Give the preparation type.
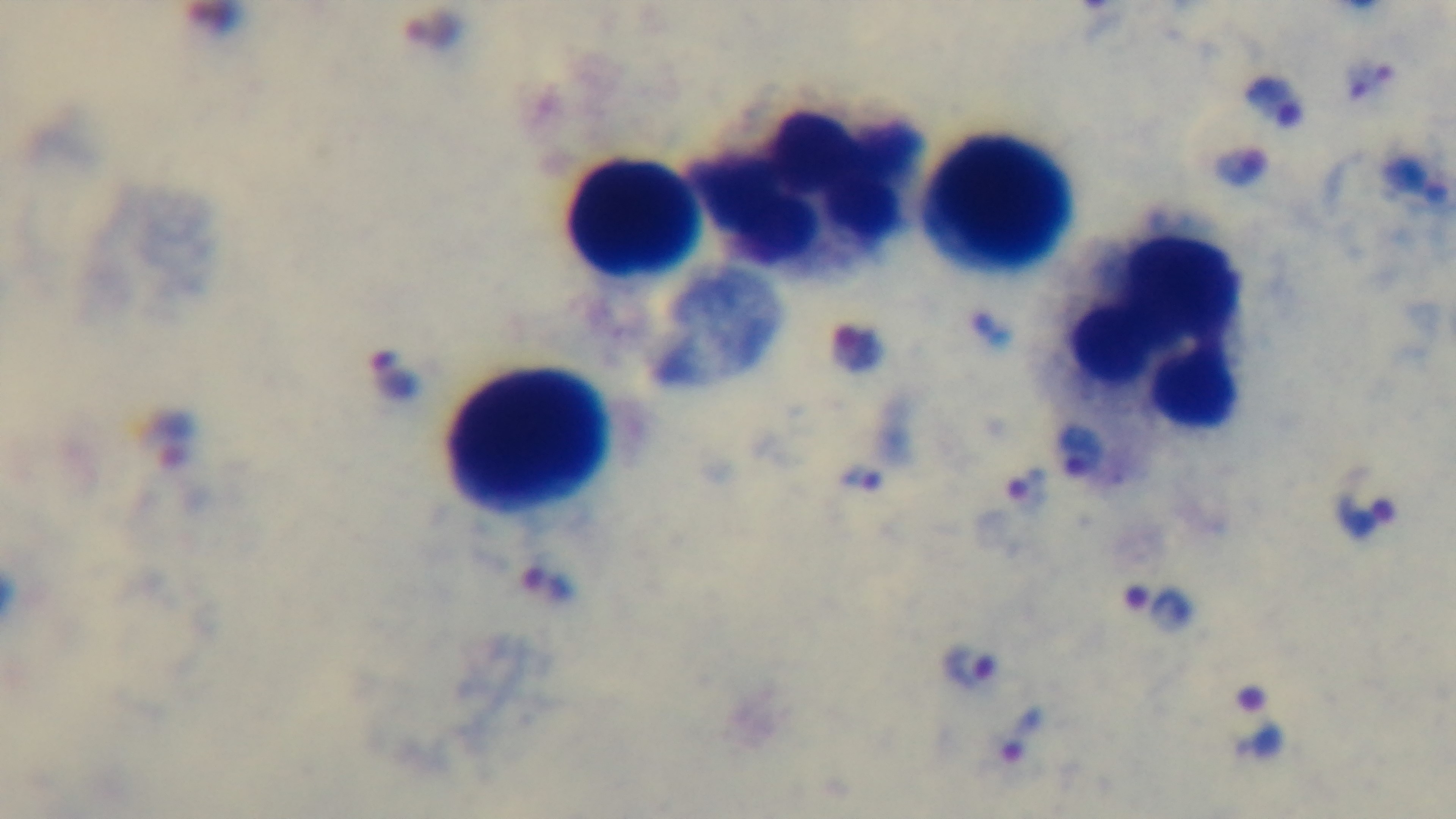
A thick smear.

Summary:
  - Stain: Giemsa
  - Capture: mounted 4K digital camera
  - Malaria status: positive
  - Modality: light microscopy
  - Field of view: single
  - Objective: 100x oil immersion